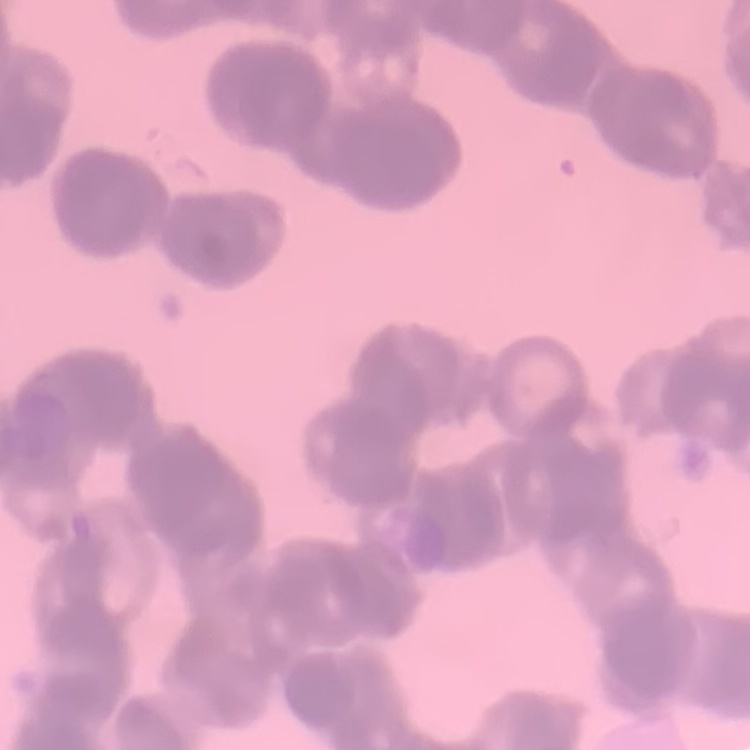

Summary:
  - Erythrocyte morphology: rouleaux formation
  - Image type: square crop of a larger photomicrograph
  - Preparation: thin peripheral smear
  - Stain: Field's or Giemsa